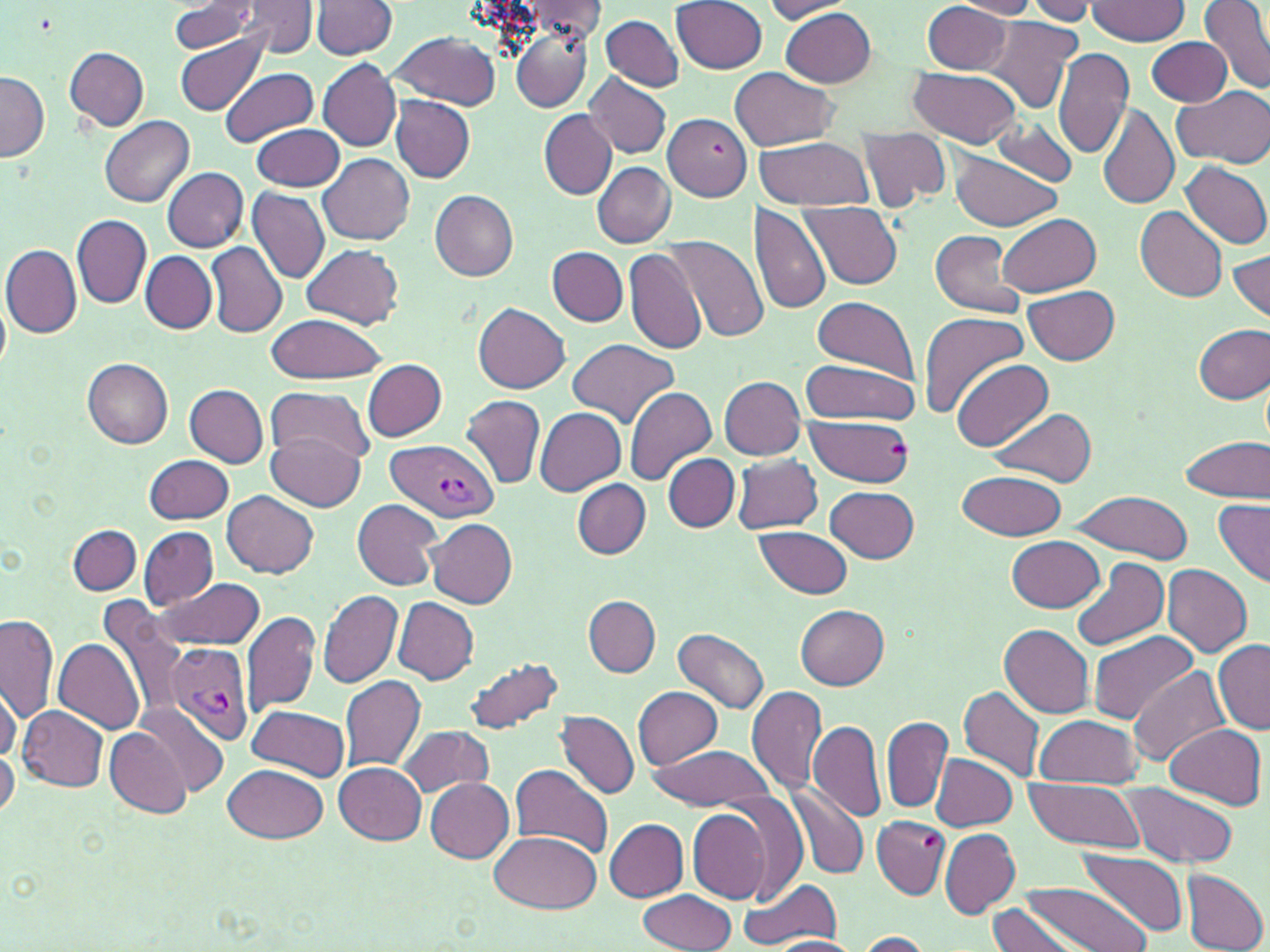

Approximate bounding boxes as (x1,y1)-(x2,y2) corner pairs in pixels. Plasmodium vivax-infected red blood cell locations: (385,440)-(497,523), (163,641)-(254,748). Uninfected red blood cell locations: (948,0)-(1042,18), (1025,0)-(1096,23), (1200,0)-(1270,93), (233,1)-(321,58), (312,1)-(397,58), (522,1)-(608,42), (673,1)-(768,73), (761,1)-(859,22), (923,1)-(1016,74), (1087,1)-(1190,46), (170,2)-(259,54), (780,7)-(877,87), (600,13)-(685,91), (982,16)-(1081,113), (511,28)-(592,112), (174,29)-(270,117), (389,30)-(502,110), (1146,36)-(1232,107), (64,47)-(150,131), (1053,49)-(1134,159), (1073,56)-(1169,192), (319,59)-(402,150), (908,66)-(1022,149), (220,67)-(320,147), (730,67)-(841,149), (1,72)-(50,162), (583,72)-(672,159), (1172,86)-(1270,167), (391,96)-(475,183), (1097,103)-(1179,209), (539,111)-(616,198), (663,113)-(750,199), (101,116)-(195,207), (987,120)-(1079,186), (250,124)-(344,191), (857,128)-(951,211), (755,136)-(874,209), (947,152)-(1066,231), (319,154)-(415,244), (1181,161)-(1270,249), (593,162)-(675,247), (163,167)-(248,252), (247,186)-(330,283), (431,190)-(518,280), (801,201)-(903,290), (749,204)-(832,315), (1135,206)-(1227,303), (72,214)-(151,309), (996,214)-(1101,296), (931,229)-(1025,318), (668,235)-(768,342), (205,241)-(288,339), (301,243)-(405,328), (2,244)-(81,338), (623,246)-(707,356), (547,247)-(627,325), (1228,247)-(1270,326), (141,250)-(215,334), (1025,285)-(1120,365), (1,293)-(11,374), (811,295)-(919,386), (474,304)-(570,393), (917,311)-(1030,417), (263,314)-(389,384), (1193,323)-(1270,404), (566,338)-(678,427), (951,357)-(1054,451), (82,359)-(174,449), (362,359)-(447,441), (798,360)-(920,425), (719,376)-(806,459), (184,384)-(269,467), (265,385)-(376,462), (623,386)-(718,486), (461,395)-(545,489), (535,407)-(626,495), (991,408)-(1097,486), (804,415)-(914,485), (265,431)-(366,510), (1181,437)-(1268,502), (145,454)-(233,524), (664,455)-(738,532), (732,455)-(822,533), (956,470)-(1066,540), (572,480)-(651,559), (826,486)-(919,563), (223,490)-(319,577), (1072,492)-(1192,563), (352,499)-(444,591), (1213,500)-(1269,589), (426,518)-(516,608), (68,524)-(142,594), (755,525)-(853,600), (139,526)-(217,609), (1008,537)-(1106,612), (1070,557)-(1169,653), (1161,565)-(1253,657), (154,579)-(263,650), (318,591)-(403,689), (584,596)-(660,676), (394,597)-(478,684), (102,599)-(187,722), (795,604)-(890,688), (241,610)-(320,716), (1,613)-(59,722), (999,624)-(1095,717), (675,627)-(770,714), (1087,630)-(1199,725), (54,638)-(145,734), (1213,641)-(1270,735), (463,655)-(566,737), (1130,666)-(1232,769), (340,676)-(426,771), (1,680)-(21,765), (746,684)-(826,796), (633,685)-(723,769), (959,685)-(1044,782), (135,703)-(229,800), (246,704)-(351,778), (20,706)-(107,792), (557,711)-(639,798), (881,714)-(953,815), (1031,715)-(1143,788), (810,721)-(886,821), (1165,724)-(1266,808), (106,726)-(194,816), (401,726)-(494,798), (0,744)-(18,821), (645,744)-(776,810), (931,753)-(1018,832), (332,762)-(426,845), (510,763)-(613,859), (225,764)-(328,843), (1023,777)-(1146,855), (425,778)-(515,863), (1125,784)-(1241,869), (789,787)-(870,880), (688,808)-(774,905), (871,817)-(948,899), (604,819)-(688,901), (940,829)-(1019,918), (490,830)-(603,913), (1081,849)-(1189,935), (1181,869)-(1269,952), (738,877)-(842,950), (1018,880)-(1153,952), (638,889)-(738,952), (989,903)-(1078,952), (855,931)-(934,951), (768,936)-(862,951). Slide-level diagnosis: Plasmodium vivax. Optical microscopy. May-Grünwald-Giemsa stain. Thin blood smear. Image is 1270×952 pixels. One field of a larger specimen. Captured at 1000x magnification.